Report the malaria status of this cell.
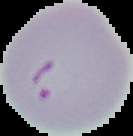
It is parasitized.

Image is 133×136 pixels. From a thin blood smear. The area outside the segmented cell region is set to black.